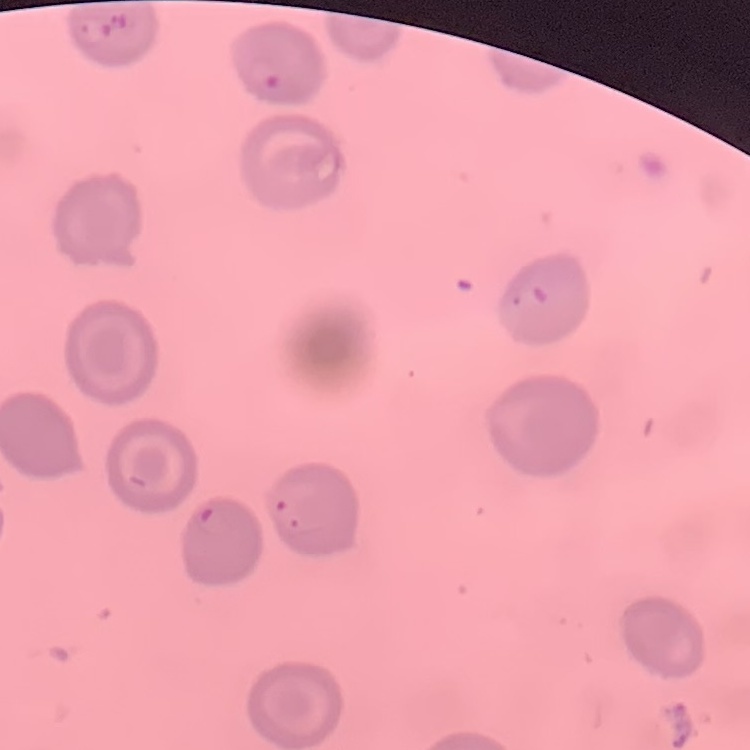
The erythrocytes exhibit no rouleaux formation. Thin peripheral smear. Square crop of a larger photomicrograph. Stained with either Field's or Giemsa.